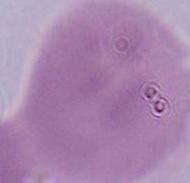

A red blood cell is seen. 1000x magnification. Micrograph.